Classify this cell by malaria status.
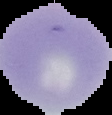

It is uninfected.

image size = 112×115 pixels
image type = segmented cell region with the area outside set to black
preparation = thin blood smear